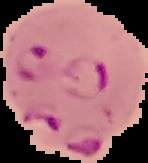

Summary:
  - Image type: segmented cell region on a black background
  - Preparation: thin blood smear
  - Image size: 148×163 pixels
  - Malaria status: parasitized